Report the malaria status of this cell.
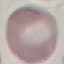
It is uninfected.

Giemsa stain. Thin blood smear. Acquired by smartphone through the microscope eyepiece. Automatically extracted cell patch, resized to 64 × 64 pixels.